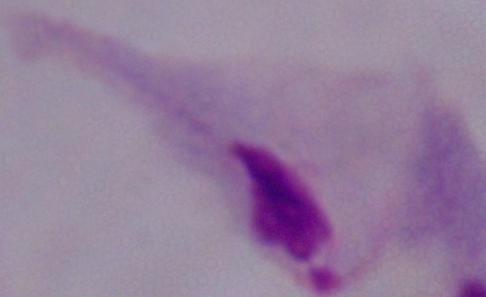
Summary:
  - Identification: trichomonad
  - Magnification: 1000x
  - Modality: photomicrograph